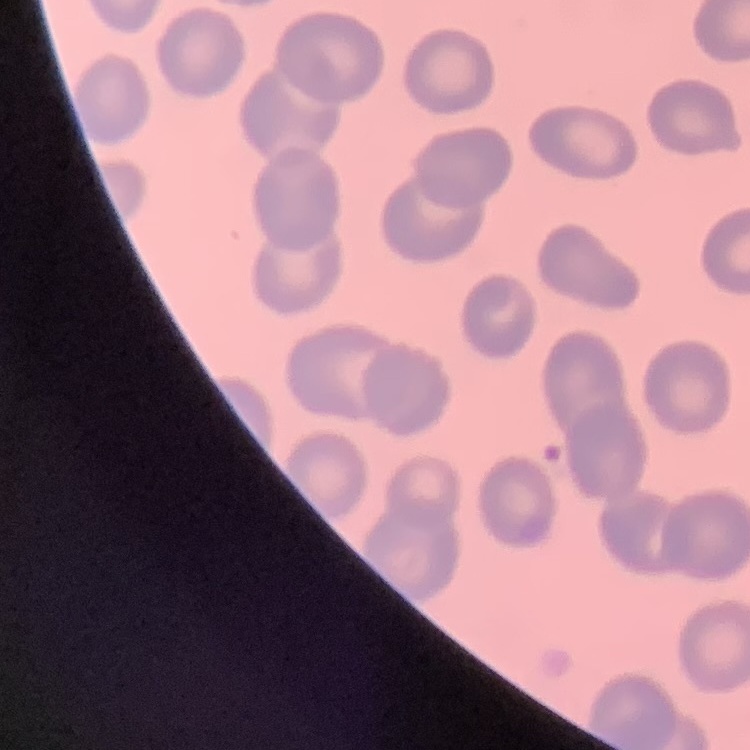

Summary:
  - Red blood cell morphology: no rouleaux formation
  - Preparation: thin blood smear
  - Image type: one tile cut from a larger photomicrograph
  - Stain: Field's or Giemsa